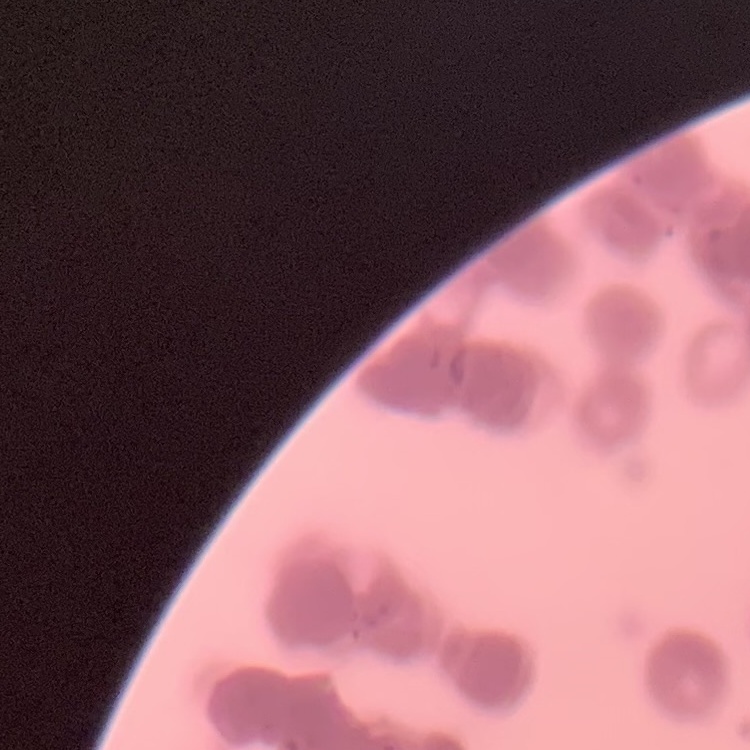
erythrocyte morphology = rouleaux formation
preparation = thin blood film
stain = Field's or Giemsa
image type = one tile cut from a larger photomicrograph